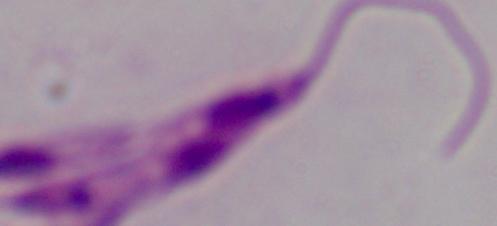
Micrograph. 1000x magnification. A Leishmania parasite is shown.